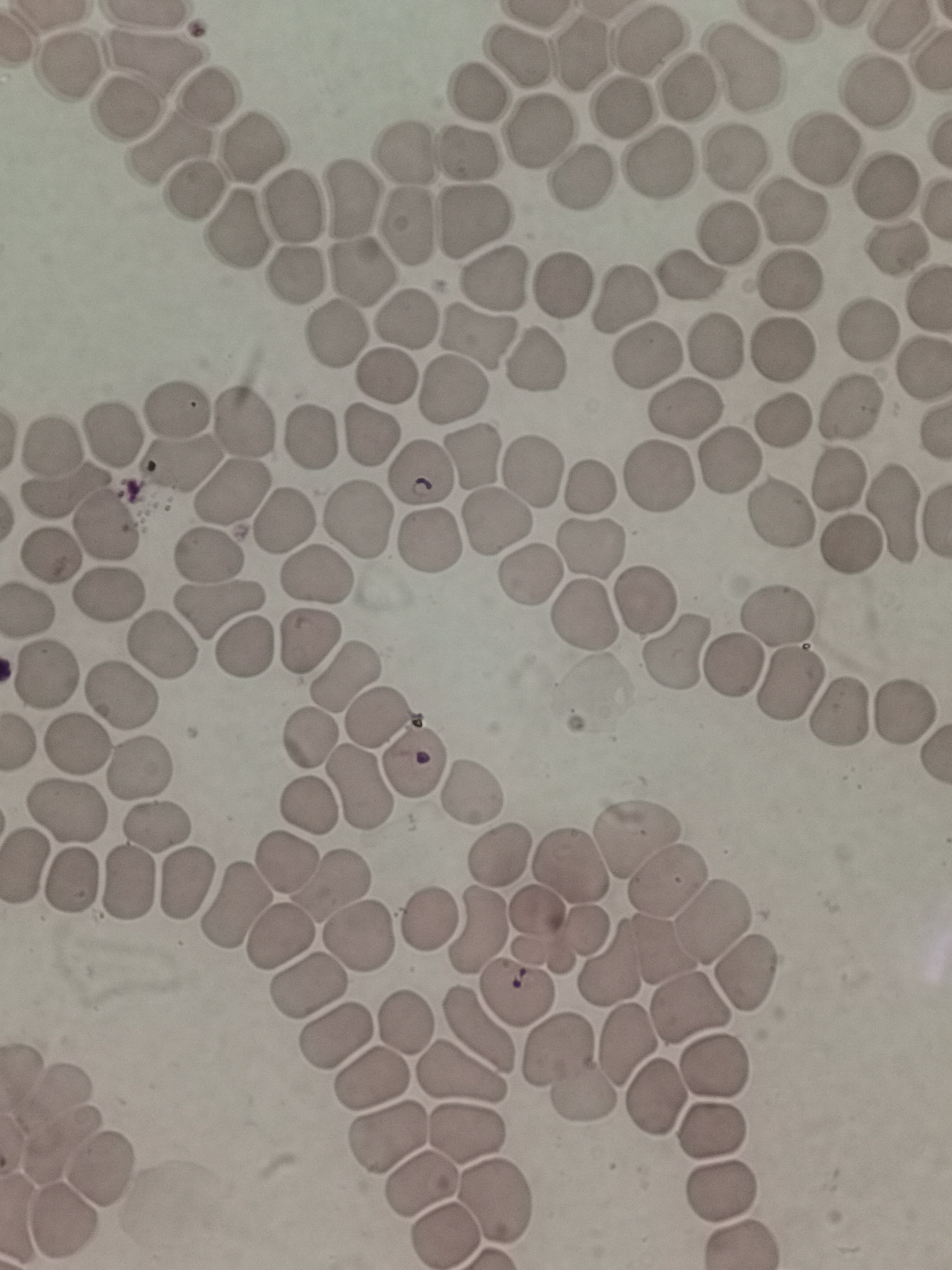

cell locations = approximate centers as (x, y) in pixels: (647, 45), (160, 49), (588, 51), (520, 52), (66, 69), (745, 71), (694, 85), (881, 89), (208, 90), (476, 93), (627, 104), (129, 108), (541, 128), (257, 140), (174, 143), (823, 149), (405, 153), (472, 153), (733, 158), (655, 162), (580, 172), (890, 184), (200, 190), (347, 195), (295, 201), (792, 216), (477, 222), (410, 223), (238, 231), (726, 235), (899, 248), (362, 267), (295, 272), (693, 274), (500, 276), (564, 285), (787, 285), (622, 298), (403, 317), (865, 330), (476, 336), (328, 340), (716, 348), (783, 353), (648, 357), (535, 360), (379, 378), (454, 393), (177, 404), (683, 408), (849, 411), (243, 421), (781, 422), (371, 433), (312, 434), (108, 436), (53, 452), (732, 458), (471, 460), (180, 465), (534, 466), (419, 476), (660, 477), (838, 480), (231, 488), (594, 488), (68, 491), (895, 510), (779, 514), (282, 518), (361, 518), (493, 521), (99, 529), (850, 544), (429, 546), (594, 548), (52, 557), (210, 559), (528, 572), (312, 579), (107, 595), (644, 600), (32, 607), (220, 608), (581, 614), (777, 618), (158, 644), (308, 644), (240, 649), (678, 650), (732, 670), (48, 676), (341, 683), (793, 683), (123, 693), (842, 712), (905, 713), (376, 718), (307, 739), (77, 745), (137, 764), (415, 764), (364, 788), (472, 791), (305, 806), (68, 814), (157, 830), (637, 837), (573, 853), (500, 858), (288, 861), (26, 866), (668, 875), (125, 879), (332, 882), (186, 883), (75, 884), (232, 906), (423, 914), (713, 922), (555, 926), (480, 927), (359, 934), (279, 939), (662, 952), (616, 968), (744, 973), (304, 984), (520, 991), (691, 1007), (402, 1021), (475, 1029), (337, 1034), (627, 1041), (715, 1063), (570, 1072), (370, 1075), (460, 1077), (656, 1098), (712, 1129), (387, 1130), (465, 1131), (103, 1166), (420, 1176), (715, 1189), (493, 1200), (62, 1221), (445, 1230)
field of view = single
capture = smartphone camera at the microscope eyepiece
preparation = thin smear
stain = Giemsa
image size = 952×1270 pixels